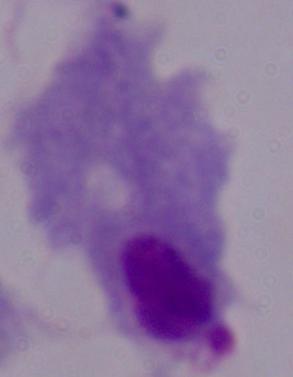

Summary:
  - Magnification: 1000x
  - Modality: micrograph
  - Identification: trichomonad